Assess the morphology of the erythrocytes.
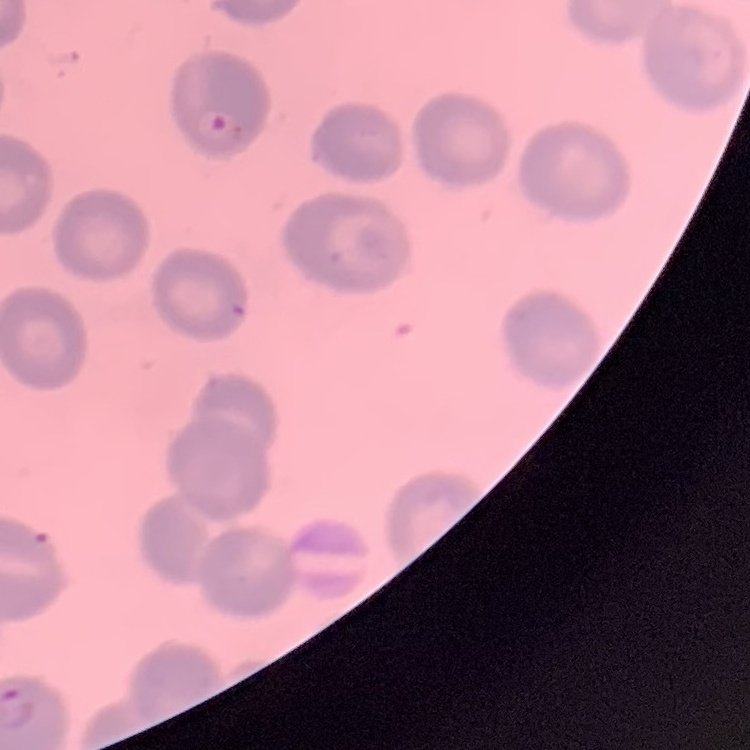

They show no rouleaux formation.

Summary:
  - Image type: one tile cut from a larger photomicrograph
  - Preparation: thin blood smear
  - Stain: Field's or Giemsa